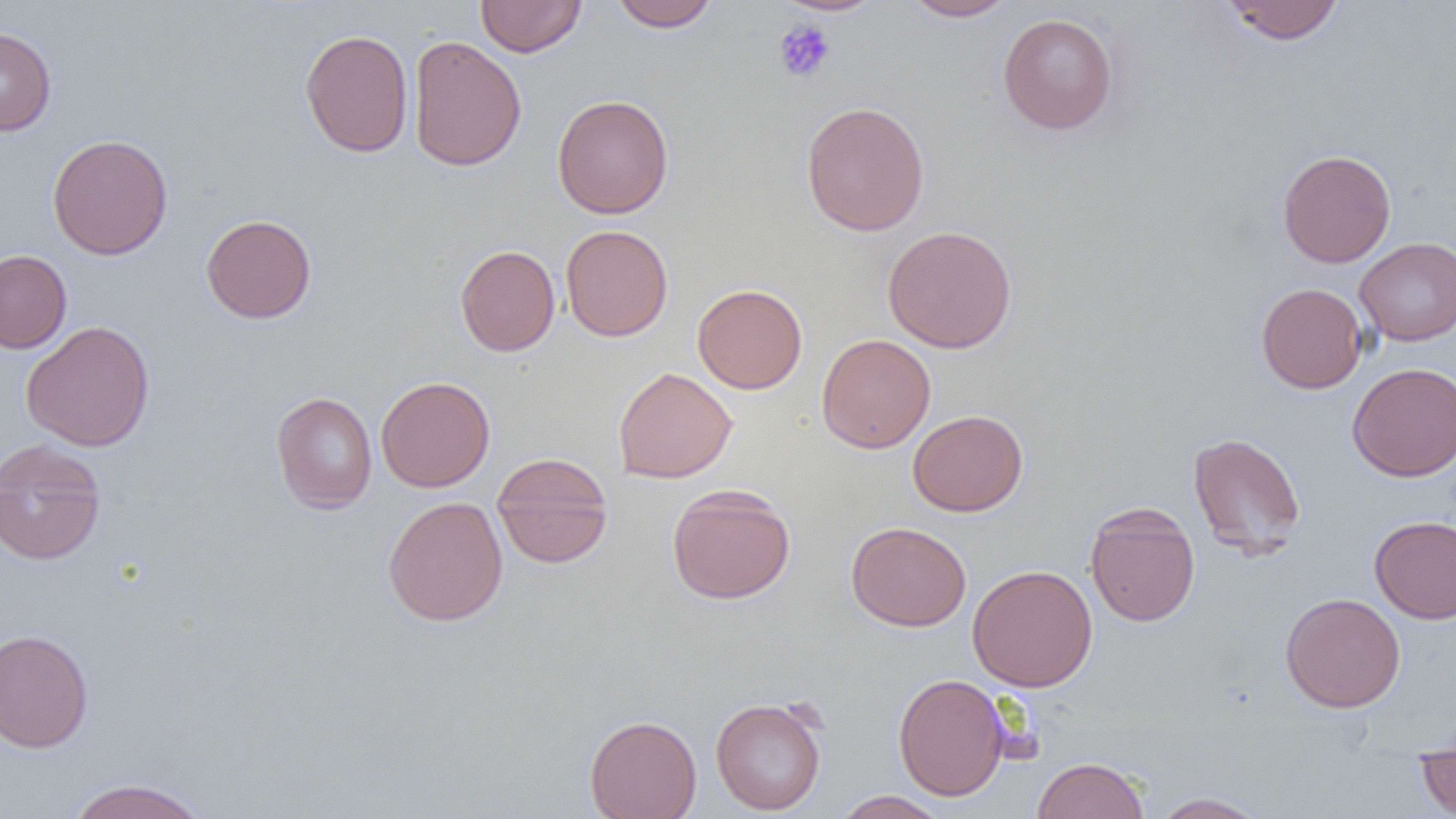
Summary:
  - Coordinate format: approximate bounding boxes as [x1, y1, x2, y2] in pixels
  - Platelet locations: [773, 19, 836, 83]
  - Uninfected red blood cell locations: [475, 0, 586, 57], [607, 0, 721, 32], [774, 0, 887, 17], [900, 0, 1017, 21], [1221, 0, 1345, 45], [998, 12, 1119, 136], [0, 26, 57, 136], [300, 28, 414, 158], [408, 36, 526, 171], [551, 94, 674, 218], [801, 100, 930, 236], [47, 133, 173, 260], [1277, 148, 1396, 268], [200, 213, 317, 324], [560, 224, 673, 342], [882, 225, 1018, 353], [1355, 237, 1456, 345], [454, 242, 674, 348], [455, 244, 560, 356], [0, 250, 72, 354], [1256, 282, 1368, 394], [692, 283, 807, 394], [21, 320, 155, 452], [816, 333, 936, 453], [1347, 362, 1456, 481], [613, 366, 737, 484], [375, 375, 495, 492], [270, 391, 377, 514], [907, 409, 1027, 517], [1187, 431, 1306, 557], [0, 439, 107, 566], [492, 452, 614, 568], [666, 484, 796, 605], [382, 496, 508, 626], [1084, 502, 1200, 627], [1369, 515, 1456, 624], [846, 521, 971, 632], [967, 564, 1098, 691], [1279, 592, 1406, 713], [0, 628, 94, 753], [893, 673, 1010, 801], [710, 695, 828, 815], [585, 714, 702, 819], [1416, 736, 1456, 819], [1032, 756, 1149, 819], [66, 777, 211, 819], [833, 790, 950, 819], [1148, 791, 1272, 818]
  - Slide-level diagnosis: no evidence of blood parasites
  - Magnification: 1000x
  - Image size: 1456×819 pixels
  - Field of view: single
  - Preparation: thin blood smear
  - Modality: light microscopy